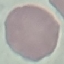

Malaria status: uninfected. Acquired by smartphone through the microscope eyepiece. Giemsa stain. Cell patch, automatically extracted from a larger field of view and resized to 64 × 64 pixels. Thin smear of blood.